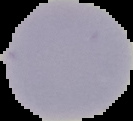
image type = segmented cell region with the area outside set to black
malaria status = uninfected
preparation = thin blood film
image size = 133×121 pixels